Report the malaria status of this cell.
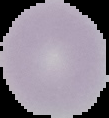
Uninfected.

Summary:
  - Preparation: thin blood film
  - Image size: 109×118 pixels
  - Image type: cell region segmented out of the field of view; surrounding area masked to black